Point out each Plasmodium parasite.
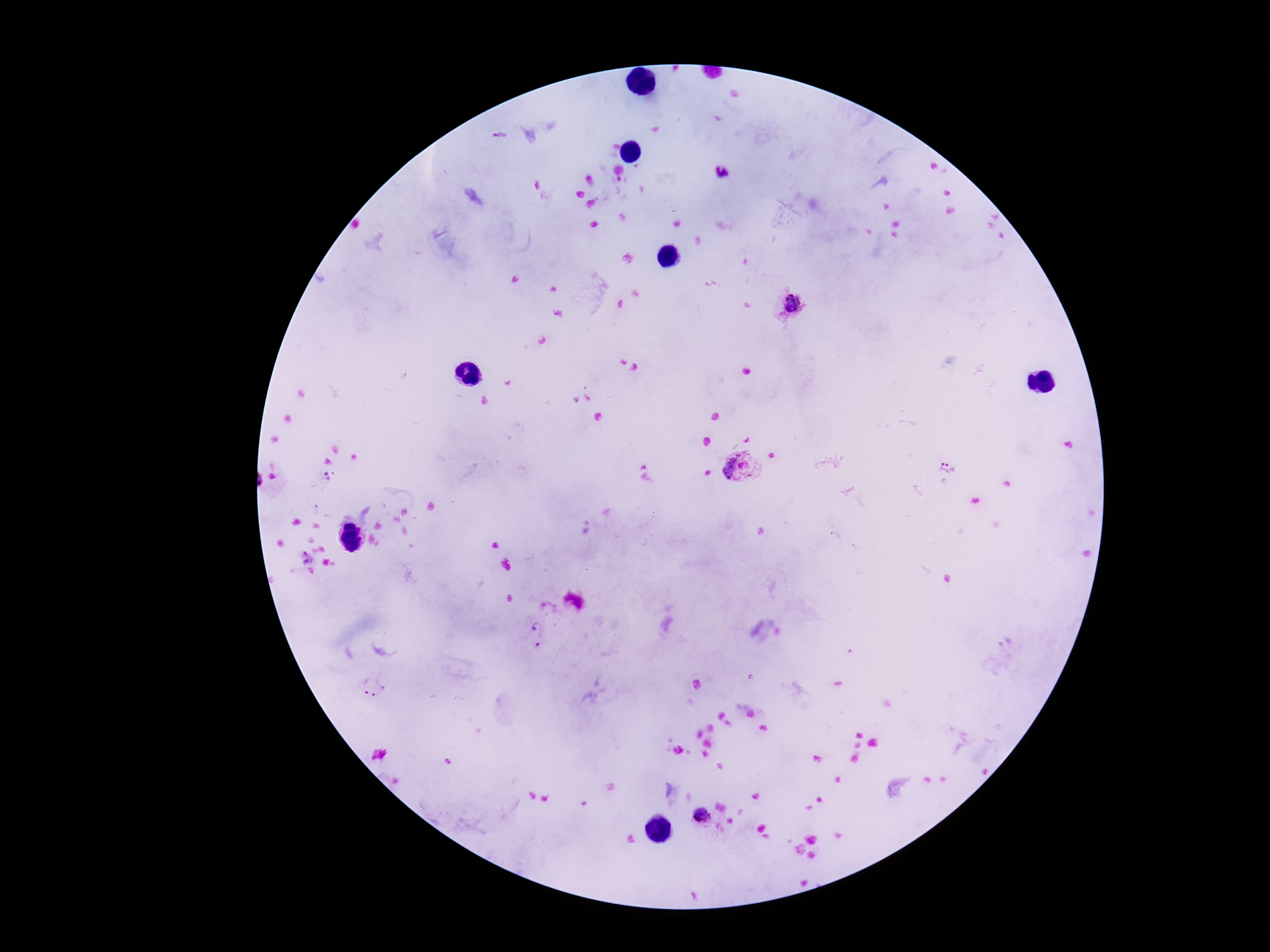
Approximate centers as (x, y) in pixels.
Plasmodium parasites: (721, 172), (793, 306), (744, 468), (948, 469), (325, 477), (307, 557), (537, 644), (373, 688), (701, 816).

Thick peripheral-blood smear. Image is 1270×952 pixels. Patient malaria status: infected. Giemsa-stained preparation. 100x magnification. Smartphone photograph taken through the microscope eyepiece. One field from this slide.